Classify this cell by malaria status.
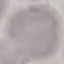
Uninfected.

image type = automatically extracted cell patch, resized to 64 × 64 pixels
preparation = thin blood smear
capture = smartphone through the microscope eyepiece
stain = Giemsa